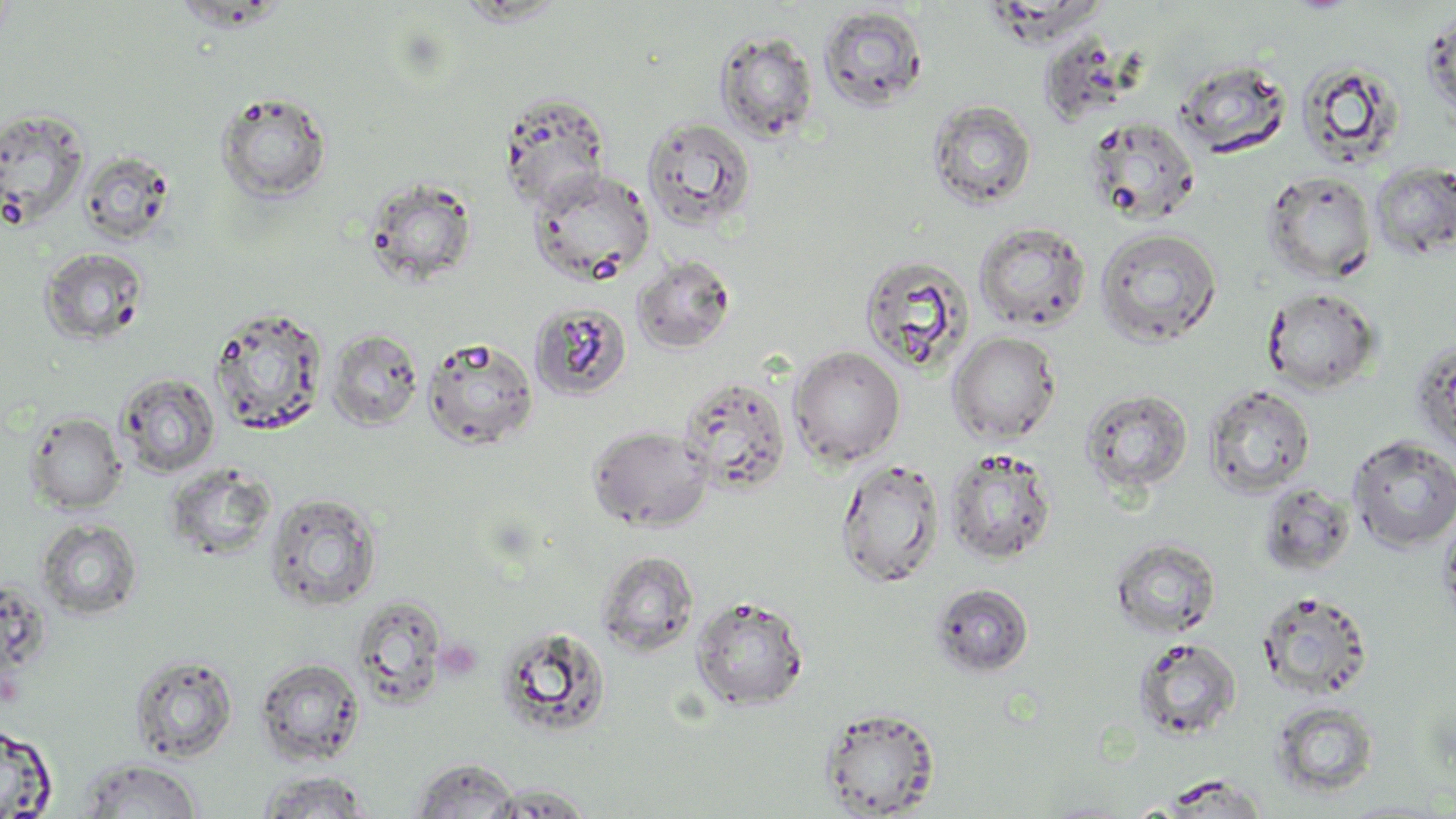

{
  "slide_level_diagnosis": "no evidence of blood parasites",
  "uninfected_red_blood_cell_locations": "approximate bounding boxes as named x1/y1/x2/y2 corners in pixels: (x1=817, y1=5, x2=929, y2=113), (x1=1423, y1=9, x2=1456, y2=127), (x1=714, y1=29, x2=819, y2=143), (x1=1174, y1=59, x2=1292, y2=159), (x1=1296, y1=59, x2=1406, y2=169), (x1=214, y1=90, x2=333, y2=204), (x1=498, y1=93, x2=611, y2=211), (x1=927, y1=99, x2=1036, y2=210), (x1=0, y1=108, x2=90, y2=229), (x1=641, y1=115, x2=757, y2=233), (x1=1083, y1=116, x2=1201, y2=227), (x1=79, y1=150, x2=175, y2=244), (x1=1370, y1=161, x2=1456, y2=259), (x1=527, y1=169, x2=657, y2=287), (x1=1263, y1=171, x2=1376, y2=283), (x1=364, y1=177, x2=478, y2=288), (x1=974, y1=221, x2=1091, y2=332), (x1=1095, y1=227, x2=1223, y2=347), (x1=39, y1=246, x2=148, y2=346), (x1=859, y1=254, x2=974, y2=374), (x1=632, y1=255, x2=736, y2=354), (x1=1262, y1=287, x2=1381, y2=394), (x1=530, y1=302, x2=632, y2=401), (x1=208, y1=304, x2=328, y2=435), (x1=327, y1=327, x2=424, y2=430), (x1=948, y1=332, x2=1061, y2=444), (x1=422, y1=337, x2=539, y2=451), (x1=1410, y1=338, x2=1456, y2=457), (x1=789, y1=345, x2=905, y2=467), (x1=116, y1=372, x2=220, y2=478), (x1=677, y1=374, x2=792, y2=495), (x1=1202, y1=383, x2=1316, y2=499), (x1=1080, y1=387, x2=1194, y2=497), (x1=25, y1=411, x2=127, y2=514), (x1=587, y1=425, x2=714, y2=532), (x1=1347, y1=435, x2=1456, y2=552), (x1=945, y1=447, x2=1057, y2=565), (x1=835, y1=458, x2=946, y2=588), (x1=166, y1=465, x2=275, y2=561), (x1=1257, y1=482, x2=1355, y2=578), (x1=264, y1=491, x2=383, y2=611), (x1=1439, y1=509, x2=1456, y2=633), (x1=36, y1=518, x2=142, y2=620), (x1=1110, y1=537, x2=1221, y2=639), (x1=596, y1=549, x2=700, y2=656), (x1=930, y1=582, x2=1034, y2=678), (x1=1256, y1=589, x2=1374, y2=701), (x1=690, y1=595, x2=810, y2=711), (x1=350, y1=596, x2=449, y2=708), (x1=495, y1=624, x2=613, y2=738), (x1=1132, y1=636, x2=1242, y2=742), (x1=129, y1=653, x2=239, y2=762), (x1=255, y1=657, x2=365, y2=765), (x1=1271, y1=701, x2=1379, y2=798), (x1=819, y1=707, x2=941, y2=818), (x1=0, y1=722, x2=58, y2=818), (x1=78, y1=758, x2=203, y2=818), (x1=409, y1=758, x2=522, y2=818), (x1=256, y1=770, x2=376, y2=817), (x1=480, y1=783, x2=595, y2=817), (x1=1336, y1=799, x2=1452, y2=817)",
  "field_of_view": "one of a larger specimen",
  "stain": "May-Grünwald-Giemsa",
  "image_size": "1456×819 pixels",
  "modality": "optical microscopy",
  "magnification": "1000x",
  "preparation": "thin blood smear"
}